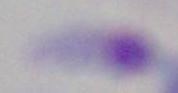
identification: Toxoplasma gondii
magnification: 1000x
modality: micrograph